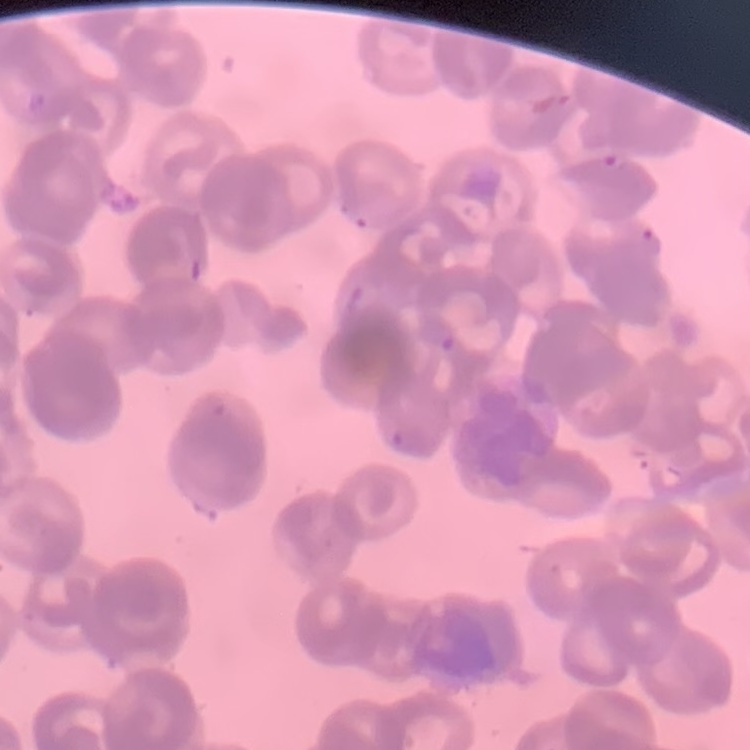

The erythrocytes show rouleaux formation. Thin peripheral smear. Stained with either Field's or Giemsa. One tile cut from a larger photomicrograph.